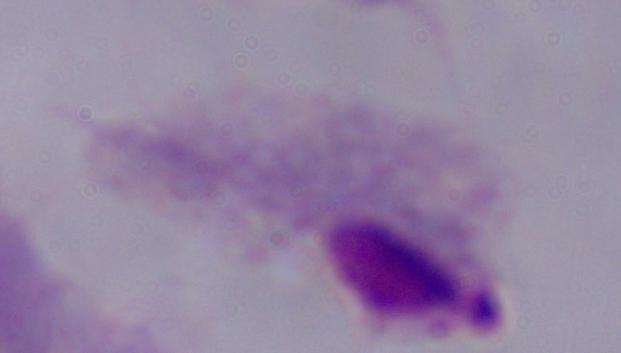
magnification: 1000x
identification: trichomonad
modality: photomicrograph